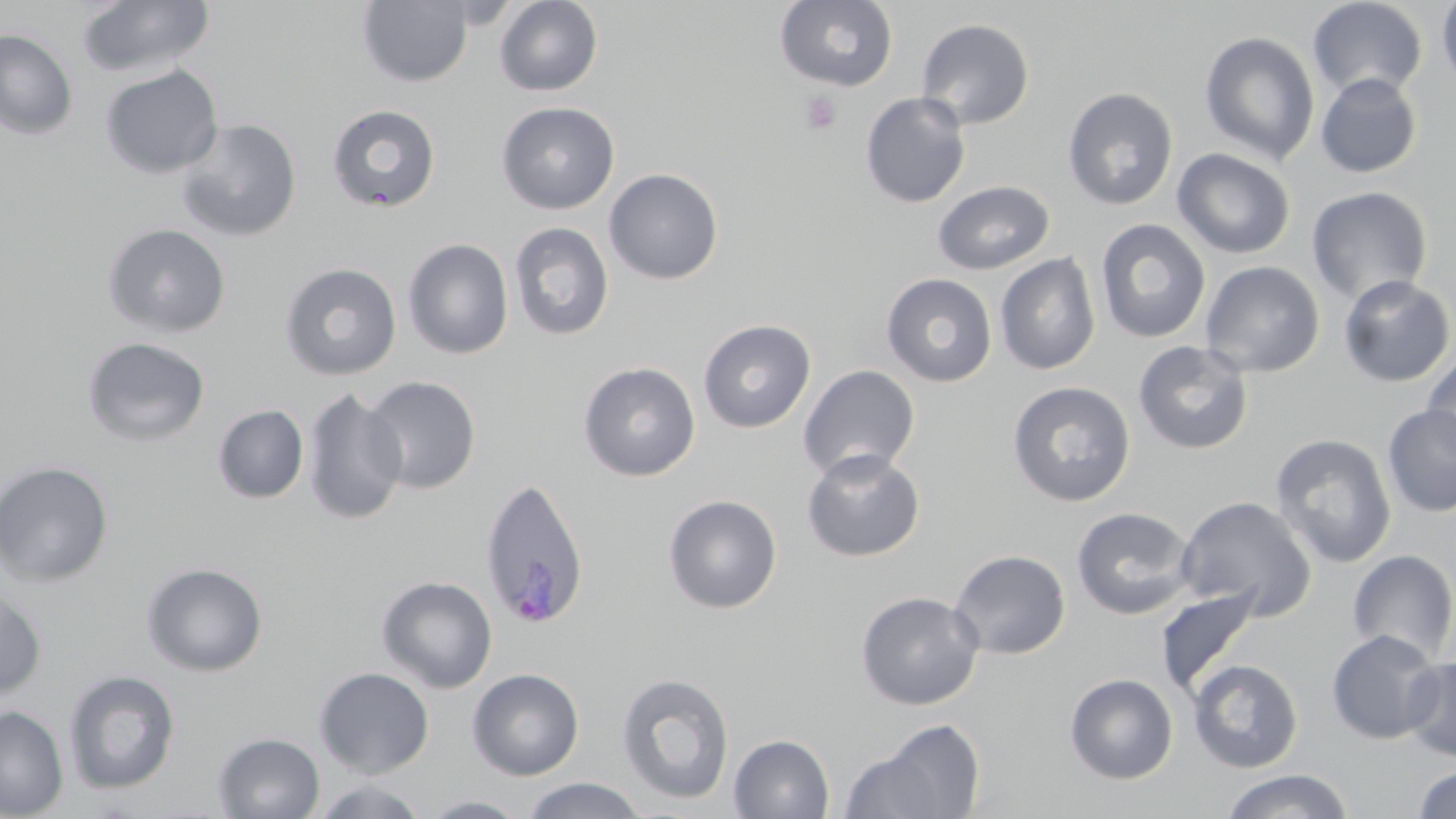
plasmodium_ovale_infected_red_blood_cell_locations: 'approximate bounding boxes as (x1, y1, x2, y2) in pixels: (478, 477, 591, 629)'
slide_level_diagnosis: Plasmodium ovale
stain: May-Grünwald-Giemsa
magnification: 1000x
uninfected_red_blood_cell_locations: 'approximate bounding boxes as (x1, y1, x2, y2) in pixels: (357, 0, 473, 87), (494, 0, 603, 96), (76, 1, 216, 78), (774, 1, 898, 91), (1307, 1, 1428, 100), (1435, 1, 1456, 91), (916, 18, 1035, 130), (0, 29, 78, 141), (1199, 30, 1320, 165), (99, 64, 223, 178), (1315, 72, 1423, 178), (1062, 87, 1178, 211), (859, 92, 971, 209), (496, 101, 620, 214), (327, 104, 441, 212), (175, 118, 302, 241), (1172, 148, 1296, 259), (603, 168, 724, 285), (932, 180, 1055, 274), (1306, 186, 1433, 306), (1094, 219, 1210, 344), (508, 222, 614, 341), (101, 223, 231, 338), (403, 238, 513, 359), (995, 252, 1101, 375), (1200, 261, 1325, 378), (278, 262, 402, 381), (881, 273, 998, 387), (1337, 275, 1455, 388), (697, 319, 816, 433), (82, 336, 211, 446), (1133, 340, 1254, 454), (1421, 346, 1456, 466), (577, 361, 701, 482), (797, 364, 921, 482), (362, 375, 481, 494), (1007, 381, 1136, 506), (301, 388, 408, 526), (213, 404, 309, 503), (1382, 405, 1456, 518), (1270, 433, 1397, 568), (800, 448, 926, 563), (0, 460, 114, 586), (662, 494, 783, 614), (1174, 495, 1317, 620), (1071, 507, 1197, 620), (949, 549, 1071, 660), (1347, 549, 1456, 665), (141, 562, 268, 676), (376, 575, 497, 693), (0, 586, 47, 701), (1155, 586, 1262, 699), (855, 590, 984, 711), (1325, 628, 1446, 744), (1400, 656, 1456, 762), (1187, 659, 1304, 773), (314, 667, 434, 778), (467, 668, 585, 780), (63, 669, 180, 796), (616, 671, 735, 806), (1064, 673, 1178, 784), (0, 704, 69, 818), (851, 717, 988, 819), (213, 732, 325, 818), (728, 734, 835, 818), (1412, 765, 1456, 819), (1220, 769, 1354, 819), (520, 778, 648, 818), (312, 779, 430, 818), (419, 795, 532, 818)'
modality: light microscopy
image_size: 1456×819 pixels
field_of_view: single
preparation: thin blood smear
platelet_locations: 'approximate bounding boxes as (x1, y1, x2, y2) in pixels: (799, 91, 842, 135)'